Find the cells and give the type of each one.
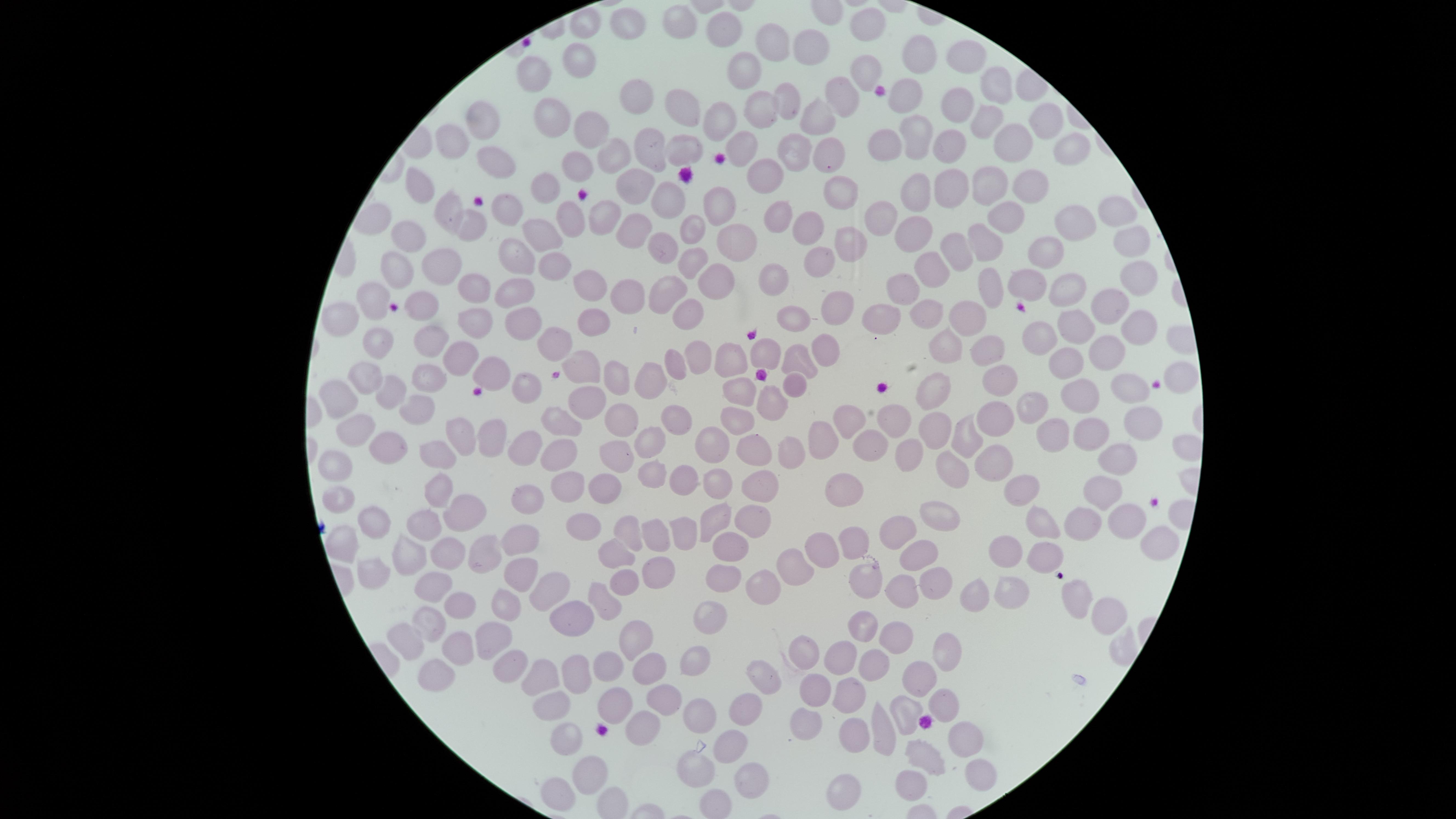

No parasitized red blood cells identified.
Approximate marker points as (x, y) in pixels.
Uninfected red blood cells: (675, 20), (587, 21), (624, 22), (864, 25), (725, 30), (776, 45), (810, 49), (924, 51), (970, 52), (576, 59), (537, 69), (745, 71), (862, 72), (990, 81), (903, 89), (844, 95), (642, 99), (786, 100), (680, 104), (956, 106), (763, 110), (550, 114), (811, 118), (987, 118), (716, 121), (482, 122), (1048, 122), (917, 126), (583, 132), (452, 138), (887, 138), (741, 145), (951, 146), (785, 147), (1015, 147), (682, 148), (821, 149), (650, 153), (613, 155), (1064, 159), (506, 160), (575, 166), (763, 169), (992, 178), (1027, 180), (947, 181), (638, 182), (421, 183), (547, 186), (916, 187), (837, 192), (668, 200), (511, 208), (718, 208), (450, 209), (781, 212), (882, 213), (1113, 215), (602, 218), (1011, 218), (568, 221), (634, 222), (804, 222), (693, 226), (469, 227), (1074, 227), (909, 230), (544, 233), (406, 235), (982, 240), (851, 241), (663, 242), (735, 243), (1124, 245), (955, 246), (1049, 246), (514, 252), (820, 256), (689, 257), (546, 259), (442, 264), (931, 264), (394, 269), (773, 275), (1130, 277), (1021, 278), (714, 279), (987, 280), (903, 284), (581, 286), (1066, 286), (467, 287), (516, 288), (664, 291), (629, 295), (379, 298), (830, 299), (1106, 304), (422, 305), (682, 308), (882, 311), (796, 312), (928, 312), (971, 312), (517, 314), (590, 314), (347, 319), (477, 319), (1078, 319), (1128, 321), (556, 335), (381, 336), (432, 336), (1041, 338), (942, 343), (823, 347), (990, 348), (1101, 351), (461, 354), (699, 355), (733, 355), (768, 355), (795, 355), (1065, 357), (584, 362), (677, 363), (491, 367), (1183, 370), (367, 376), (1003, 377), (621, 378), (655, 378), (432, 379), (799, 381), (935, 384), (533, 385), (394, 387), (1133, 387), (743, 388), (1079, 391), (347, 396), (422, 397), (586, 397), (775, 399), (1035, 399), (628, 409), (995, 414), (675, 417), (738, 419), (1145, 420), (562, 421), (843, 421), (893, 423), (361, 425), (934, 427), (1054, 427), (456, 428), (1094, 429), (487, 435), (966, 436), (652, 438), (823, 439), (868, 439), (391, 441), (712, 443), (524, 444), (566, 447), (789, 448), (756, 449), (906, 450), (620, 452), (436, 453), (1117, 456), (996, 460), (338, 461), (956, 469), (653, 471), (678, 482), (719, 482), (757, 485), (566, 486), (605, 488), (1022, 488), (442, 490), (843, 491), (1106, 492), (531, 496), (344, 502), (465, 509), (940, 513), (714, 518), (747, 518), (376, 519), (1128, 519), (1046, 520), (1088, 522), (583, 524), (630, 524), (421, 528), (891, 530), (679, 531), (656, 534), (522, 537), (1156, 540), (849, 542), (730, 544), (339, 548), (617, 548), (1002, 550), (408, 551), (914, 551), (825, 552), (1041, 552), (448, 553), (486, 553), (517, 565), (800, 566), (368, 567), (653, 571), (720, 577), (866, 580), (627, 581), (760, 583), (937, 583), (549, 585), (439, 586), (968, 589), (1008, 589), (899, 591), (1075, 596), (608, 601), (456, 603), (505, 605), (572, 611), (1101, 612), (708, 613), (425, 623), (860, 625), (891, 628), (629, 634), (492, 639), (406, 641), (459, 646), (809, 651), (949, 651), (841, 654), (692, 662), (510, 664), (569, 665), (604, 666), (874, 667), (650, 671), (435, 673), (920, 676), (540, 678), (765, 678), (662, 692), (846, 693), (814, 694), (945, 701), (551, 704), (615, 707), (742, 708), (694, 711), (904, 714), (644, 719), (806, 725), (853, 727), (881, 733), (565, 736), (962, 736), (728, 742), (920, 759), (584, 769), (692, 769), (747, 769), (977, 769), (910, 778), (558, 785), (844, 791), (718, 803).
No white blood cells identified.

Single field of view. Smartphone photograph through the microscope eyepiece. Giemsa stain. Image is 1456×819 pixels. Thin blood film. The visible region is circular.